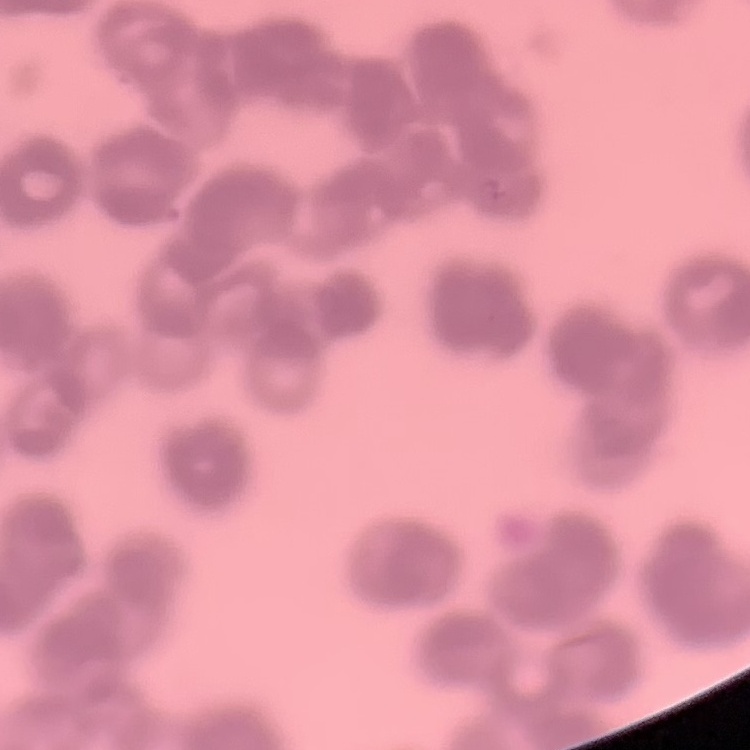

erythrocyte morphology = rouleaux formation
stain = Field's or Giemsa
image type = square crop of a larger photomicrograph
preparation = thin blood smear